Assess for parasitized red blood cells.
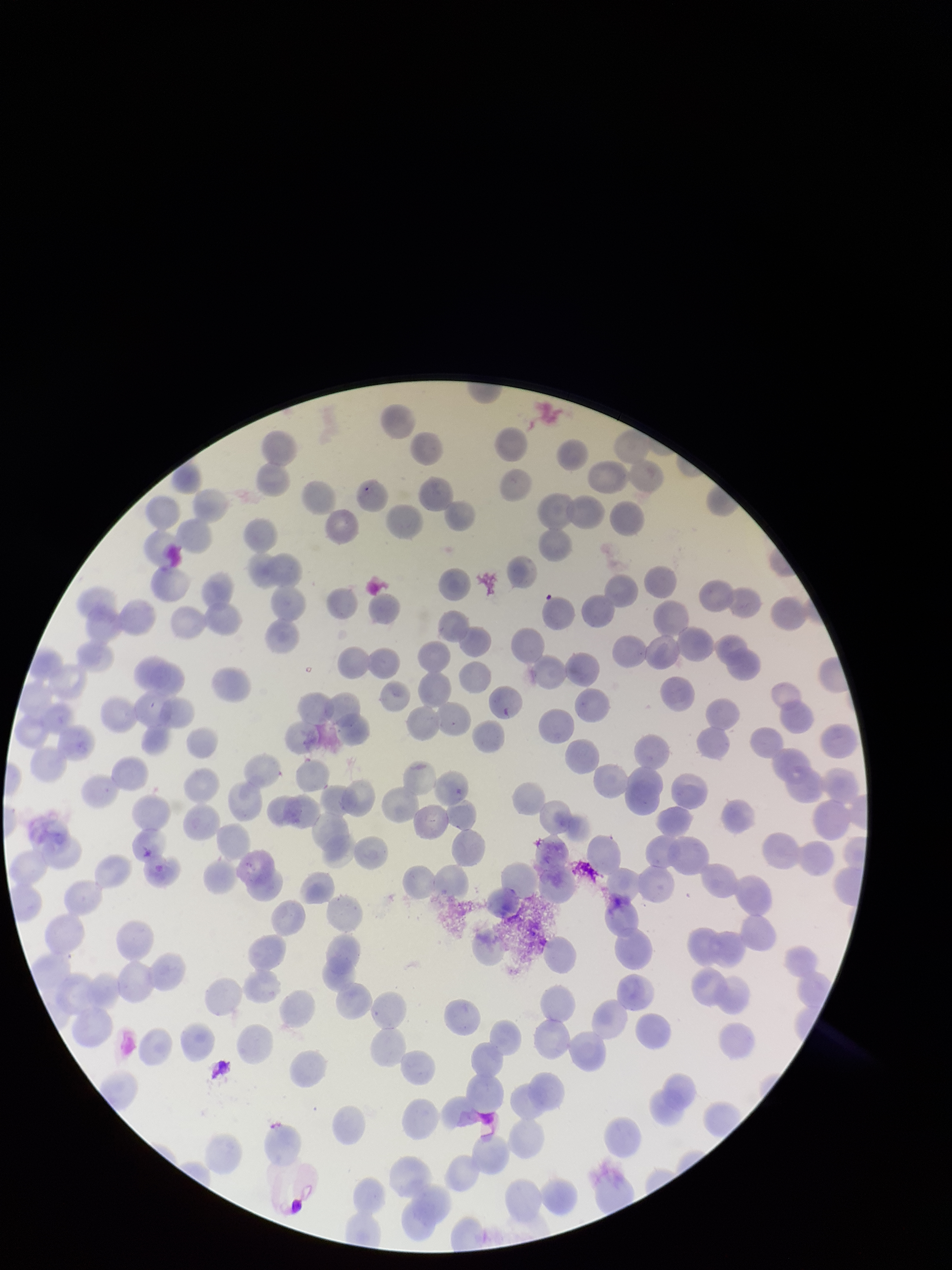
None seen.

image_size: 952×1270 pixels
parasitized_red_blood_cell_count: 0
stain: Giemsa
field_of_view: one from this slide
preparation: thin smear
capture: smartphone photograph through the microscope eyepiece
patient_malaria_status: positive
red_blood_cell_count: 209
species_reported_for_this_patient: Plasmodium falciparum